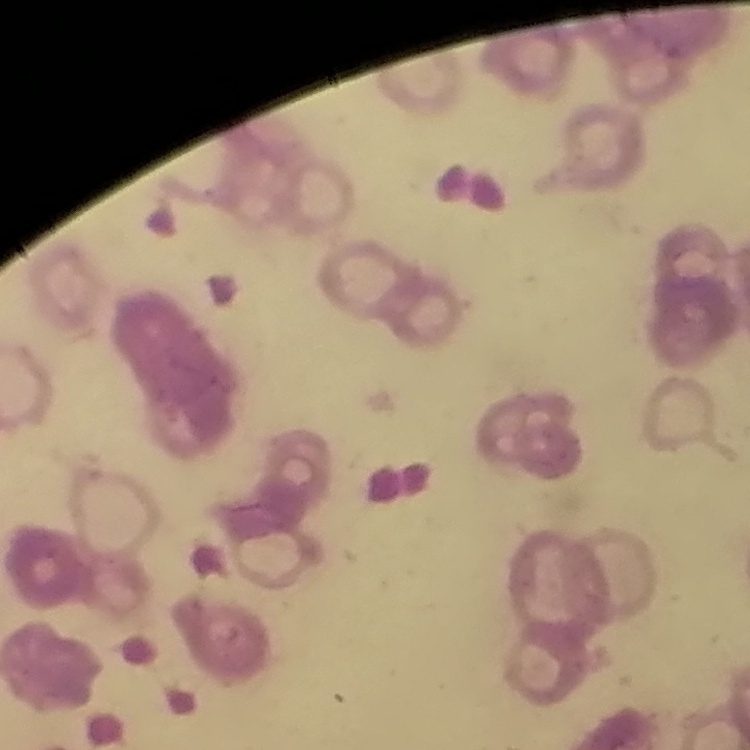
Summary:
  - Red blood cell morphology: rouleaux formation
  - Stain: Field's or Giemsa
  - Image type: one tile cut from a larger photomicrograph
  - Preparation: thin peripheral smear